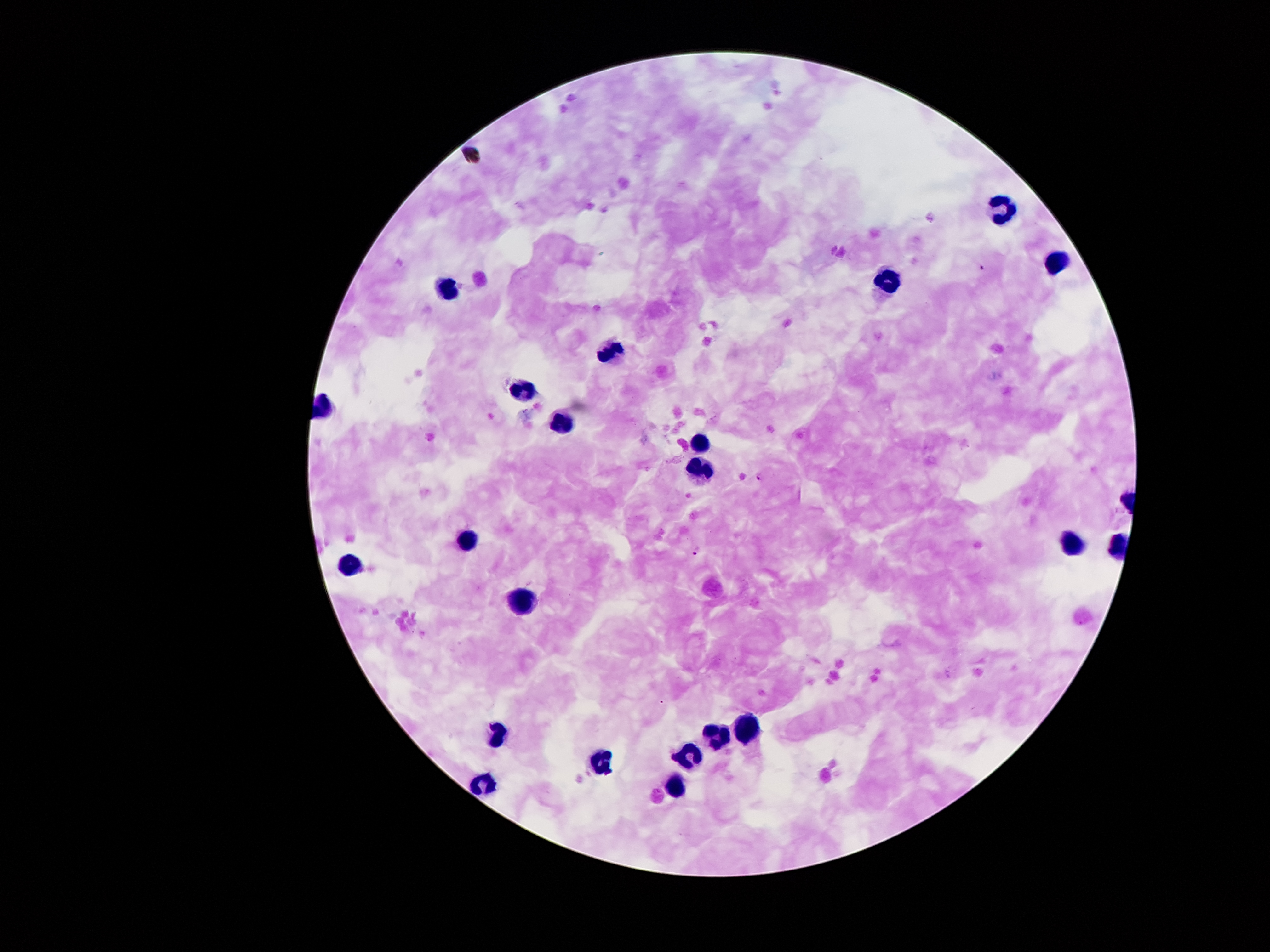
image_size: 1270×952 pixels
capture: smartphone through the microscope eyepiece
field_of_view: single
preparation: thick blood smear
malaria_parasite_locations: 'approximate centers as [x, y] in pixels: [983, 268], [761, 476], [697, 551]'
magnification: 100x
patient_malaria_status: positive for Plasmodium falciparum
stain: Giemsa
leukocyte_locations: 'approximate centers as [x, y] in pixels: [1002, 208], [1057, 262], [886, 283], [447, 288], [608, 351], [523, 392], [561, 421], [700, 445], [702, 472], [466, 538], [1070, 542], [349, 559], [523, 600], [745, 731], [496, 735], [716, 737], [689, 754], [601, 764], [672, 783], [481, 787]'